Name the cell type shown.
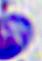

A leukocyte.

Summary:
  - Magnification: 400x
  - Modality: photomicrograph